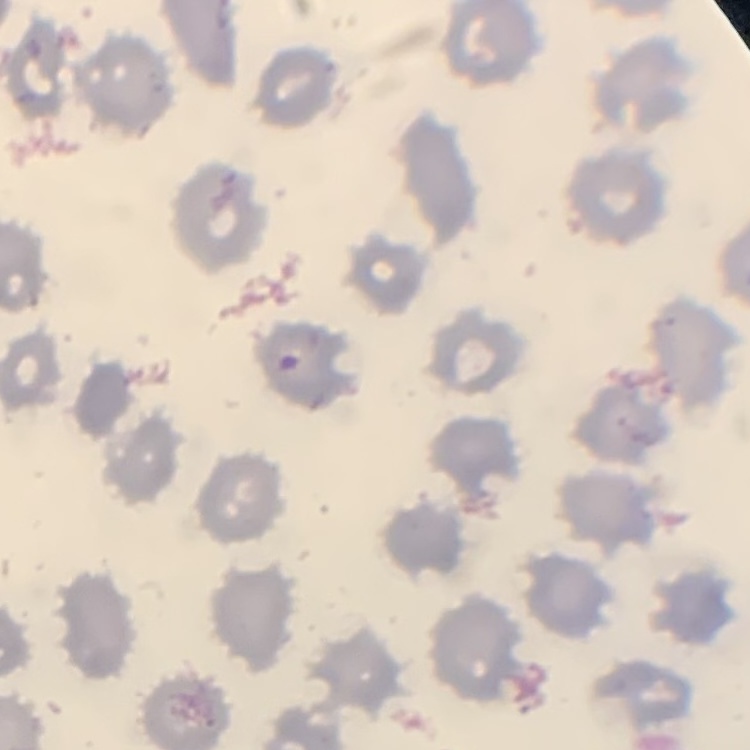
erythrocyte morphology = no rouleaux formation
stain = Field's or Giemsa
preparation = thin blood smear
image type = one tile cut from a larger photomicrograph